Report the malaria status of this cell.
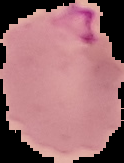

It is parasitized.

image size = 124×163 pixels
image type = cell region segmented out of the field of view; surrounding area masked to black
preparation = thin blood film